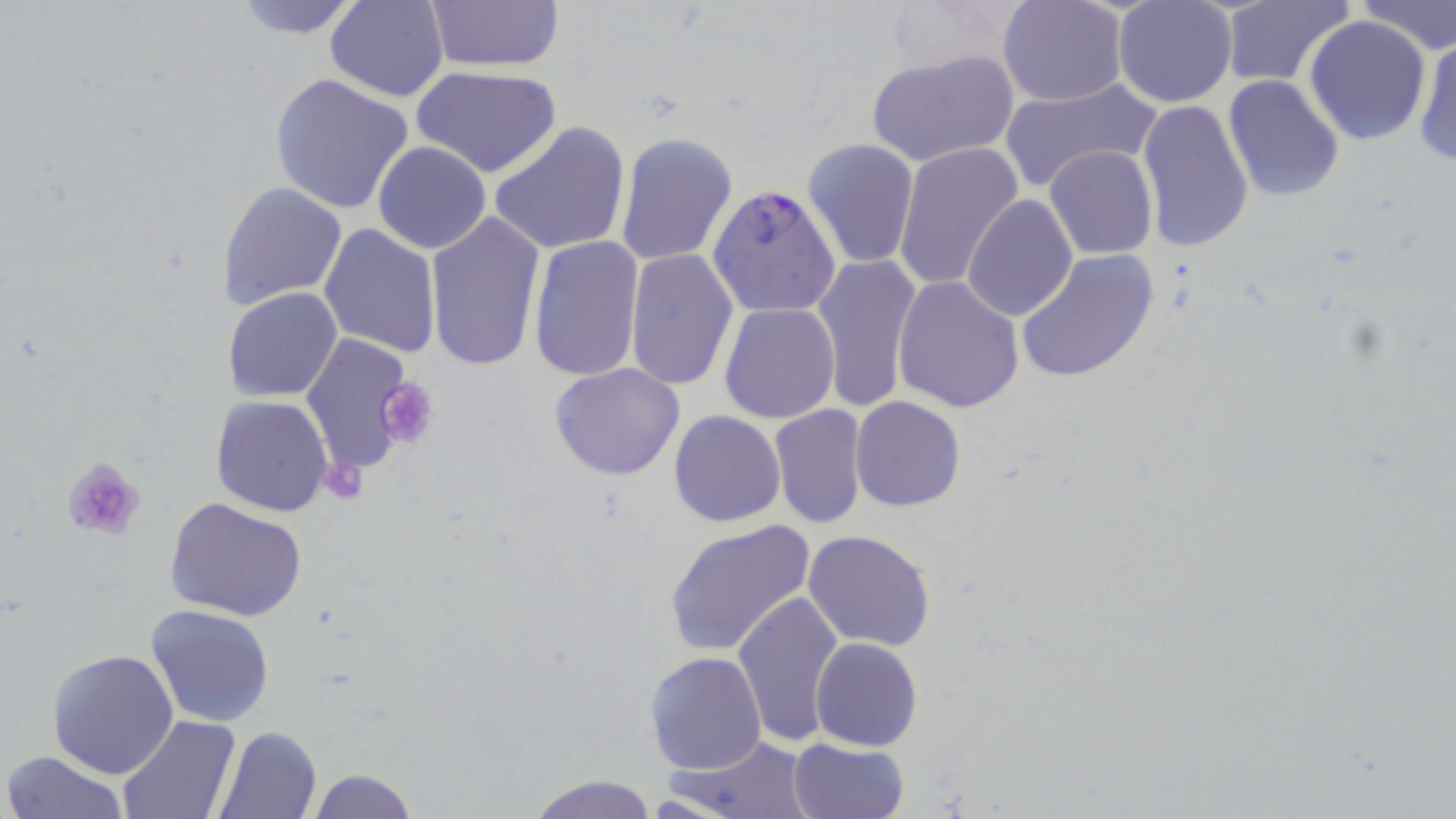 Approximate bounding boxes as named x1/y1/x2/y2 corners in pixels. Uninfected red blood cell locations: (x1=226, y1=0, x2=368, y2=40), (x1=324, y1=0, x2=449, y2=101), (x1=423, y1=0, x2=566, y2=73), (x1=881, y1=0, x2=1020, y2=74), (x1=998, y1=0, x2=1127, y2=106), (x1=1113, y1=0, x2=1236, y2=107), (x1=1357, y1=1, x2=1455, y2=55), (x1=1218, y1=2, x2=1353, y2=87), (x1=1305, y1=16, x2=1433, y2=145), (x1=1412, y1=30, x2=1456, y2=167), (x1=866, y1=51, x2=1018, y2=168), (x1=411, y1=64, x2=562, y2=177), (x1=271, y1=73, x2=411, y2=215), (x1=1223, y1=76, x2=1346, y2=204), (x1=1000, y1=78, x2=1162, y2=190), (x1=1136, y1=98, x2=1254, y2=254), (x1=488, y1=121, x2=631, y2=255), (x1=615, y1=131, x2=740, y2=266), (x1=803, y1=138, x2=921, y2=269), (x1=372, y1=141, x2=491, y2=254), (x1=894, y1=142, x2=1023, y2=293), (x1=1044, y1=146, x2=1157, y2=260), (x1=218, y1=181, x2=348, y2=308), (x1=963, y1=192, x2=1079, y2=322), (x1=424, y1=208, x2=545, y2=372), (x1=319, y1=222, x2=440, y2=359), (x1=528, y1=233, x2=644, y2=381), (x1=625, y1=250, x2=740, y2=393), (x1=1016, y1=250, x2=1160, y2=384), (x1=811, y1=253, x2=921, y2=413), (x1=893, y1=275, x2=1025, y2=414), (x1=224, y1=287, x2=344, y2=402), (x1=720, y1=302, x2=839, y2=424), (x1=299, y1=331, x2=418, y2=481), (x1=550, y1=364, x2=687, y2=481), (x1=211, y1=395, x2=335, y2=517), (x1=850, y1=395, x2=965, y2=511), (x1=768, y1=404, x2=870, y2=529), (x1=669, y1=410, x2=786, y2=527), (x1=164, y1=495, x2=308, y2=621), (x1=665, y1=519, x2=815, y2=656), (x1=803, y1=529, x2=935, y2=649), (x1=733, y1=587, x2=847, y2=747), (x1=145, y1=603, x2=275, y2=728), (x1=810, y1=637, x2=922, y2=751), (x1=48, y1=648, x2=179, y2=778), (x1=645, y1=650, x2=766, y2=776), (x1=114, y1=714, x2=238, y2=819), (x1=214, y1=726, x2=322, y2=818), (x1=663, y1=734, x2=817, y2=818), (x1=788, y1=737, x2=908, y2=819), (x1=2, y1=749, x2=129, y2=819), (x1=308, y1=767, x2=416, y2=819), (x1=528, y1=774, x2=658, y2=818). Platelet locations: (x1=374, y1=377, x2=439, y2=449), (x1=61, y1=456, x2=146, y2=543), (x1=321, y1=464, x2=369, y2=501). Plasmodium falciparum-infected red blood cell locations: (x1=708, y1=183, x2=841, y2=318). Slide-level diagnosis: Plasmodium falciparum. Image is 1456×819 pixels. 1000x magnification. One field of a larger specimen. May-Grünwald-Giemsa-stained preparation. Thin blood smear. Light microscopy.